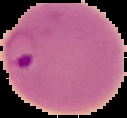
Summary:
  - Image type: segmented cell region on a black background
  - Preparation: thin blood film
  - Image size: 127×118 pixels
  - Malaria status: parasitized